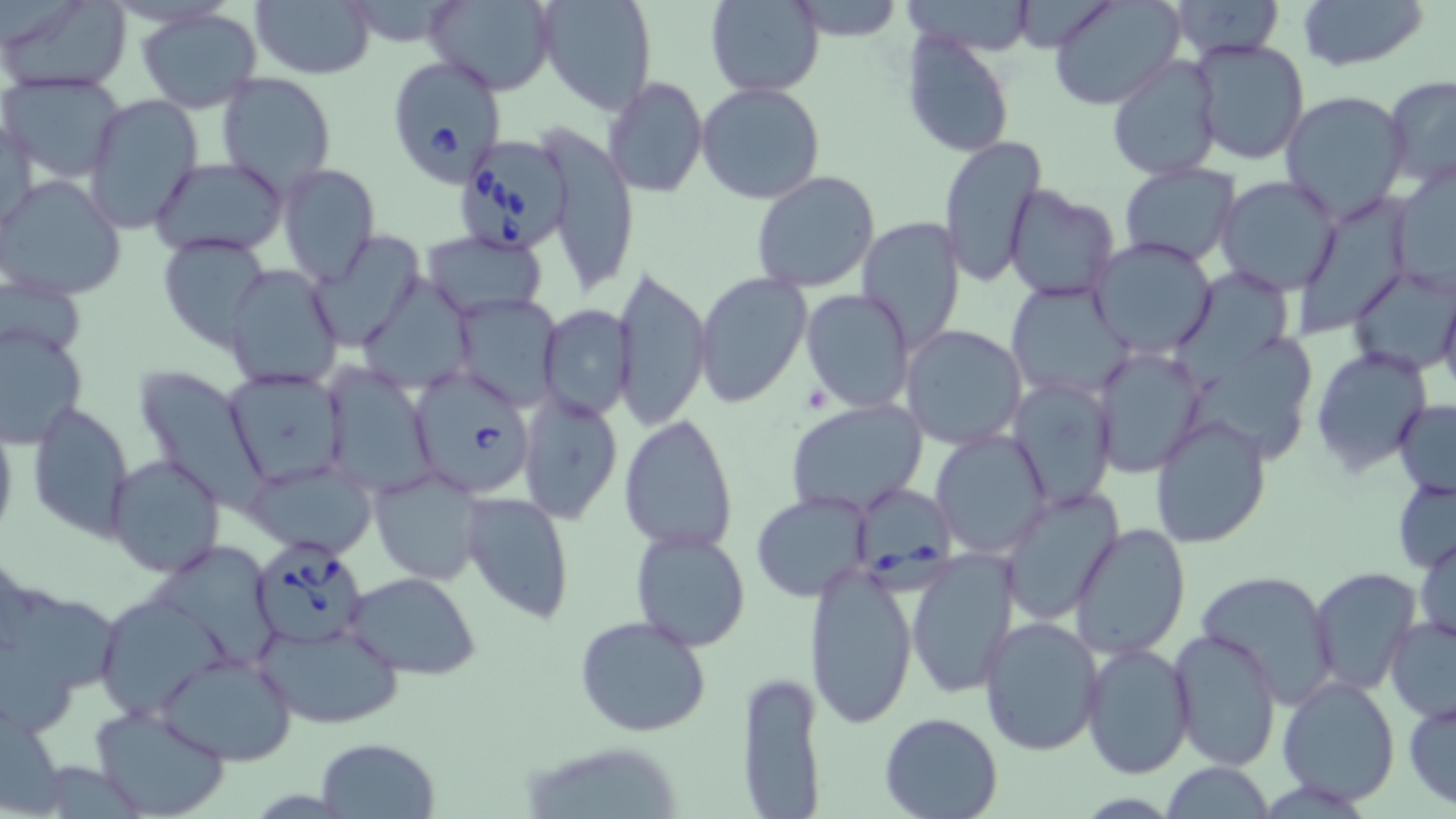

Approximate bounding boxes as named x1/y1/x2/y2 corners in pixels. Babesia divergens-infected red blood cell locations: (x1=384, y1=51, x2=506, y2=189), (x1=452, y1=130, x2=575, y2=257), (x1=405, y1=366, x2=535, y2=497), (x1=852, y1=480, x2=959, y2=596), (x1=249, y1=538, x2=368, y2=651). Platelet locations: (x1=802, y1=383, x2=829, y2=411). Uninfected red blood cell locations: (x1=1, y1=0, x2=130, y2=94), (x1=425, y1=0, x2=556, y2=94), (x1=537, y1=0, x2=657, y2=115), (x1=705, y1=0, x2=824, y2=97), (x1=1048, y1=0, x2=1182, y2=110), (x1=1298, y1=0, x2=1428, y2=70), (x1=1168, y1=1, x2=1285, y2=61), (x1=251, y1=2, x2=376, y2=79), (x1=787, y1=2, x2=909, y2=43), (x1=137, y1=8, x2=262, y2=114), (x1=900, y1=29, x2=1015, y2=160), (x1=1187, y1=38, x2=1311, y2=168), (x1=1105, y1=56, x2=1222, y2=183), (x1=215, y1=71, x2=337, y2=194), (x1=2, y1=74, x2=128, y2=182), (x1=1383, y1=74, x2=1456, y2=189), (x1=603, y1=76, x2=708, y2=199), (x1=696, y1=82, x2=826, y2=205), (x1=1282, y1=90, x2=1412, y2=224), (x1=81, y1=94, x2=202, y2=234), (x1=2, y1=113, x2=39, y2=234), (x1=543, y1=130, x2=641, y2=292), (x1=938, y1=136, x2=1047, y2=286), (x1=150, y1=157, x2=289, y2=257), (x1=277, y1=163, x2=380, y2=287), (x1=1118, y1=163, x2=1239, y2=269), (x1=1388, y1=163, x2=1456, y2=297), (x1=750, y1=171, x2=881, y2=294), (x1=0, y1=174, x2=127, y2=300), (x1=1214, y1=177, x2=1345, y2=296), (x1=1004, y1=184, x2=1121, y2=300), (x1=1302, y1=186, x2=1416, y2=334), (x1=856, y1=218, x2=969, y2=352), (x1=422, y1=231, x2=549, y2=319), (x1=308, y1=232, x2=426, y2=350), (x1=156, y1=233, x2=272, y2=350), (x1=1088, y1=237, x2=1218, y2=359), (x1=613, y1=263, x2=713, y2=431), (x1=1348, y1=264, x2=1455, y2=378), (x1=222, y1=265, x2=344, y2=390), (x1=693, y1=271, x2=813, y2=408), (x1=1, y1=275, x2=84, y2=356), (x1=1171, y1=275, x2=1296, y2=387), (x1=360, y1=280, x2=477, y2=394), (x1=1005, y1=280, x2=1133, y2=405), (x1=1439, y1=282, x2=1456, y2=403), (x1=800, y1=288, x2=915, y2=413), (x1=449, y1=294, x2=562, y2=411), (x1=539, y1=305, x2=635, y2=419), (x1=1, y1=323, x2=87, y2=446), (x1=899, y1=324, x2=1030, y2=450), (x1=1182, y1=343, x2=1312, y2=454), (x1=1311, y1=346, x2=1433, y2=474), (x1=1092, y1=347, x2=1206, y2=477), (x1=322, y1=366, x2=439, y2=497), (x1=132, y1=367, x2=269, y2=510), (x1=222, y1=368, x2=348, y2=487), (x1=1007, y1=379, x2=1117, y2=510), (x1=516, y1=391, x2=622, y2=524), (x1=786, y1=398, x2=926, y2=517), (x1=28, y1=401, x2=133, y2=538), (x1=1393, y1=401, x2=1456, y2=497), (x1=619, y1=413, x2=738, y2=552), (x1=1149, y1=413, x2=1273, y2=548), (x1=0, y1=420, x2=18, y2=543), (x1=931, y1=429, x2=1051, y2=560), (x1=105, y1=454, x2=225, y2=577), (x1=244, y1=457, x2=378, y2=558), (x1=368, y1=467, x2=485, y2=585), (x1=1392, y1=476, x2=1456, y2=573), (x1=998, y1=488, x2=1123, y2=621), (x1=751, y1=490, x2=873, y2=603), (x1=461, y1=491, x2=574, y2=625), (x1=1068, y1=524, x2=1190, y2=660), (x1=629, y1=527, x2=751, y2=653), (x1=1413, y1=534, x2=1455, y2=645), (x1=150, y1=543, x2=282, y2=665), (x1=907, y1=551, x2=1020, y2=699), (x1=803, y1=564, x2=919, y2=729), (x1=1310, y1=566, x2=1422, y2=694), (x1=1194, y1=568, x2=1339, y2=705), (x1=345, y1=572, x2=482, y2=677), (x1=20, y1=599, x2=125, y2=696), (x1=96, y1=604, x2=233, y2=717), (x1=575, y1=614, x2=712, y2=738), (x1=1385, y1=615, x2=1456, y2=723), (x1=978, y1=616, x2=1107, y2=757), (x1=255, y1=618, x2=406, y2=731), (x1=1169, y1=628, x2=1281, y2=770), (x1=1081, y1=642, x2=1195, y2=777), (x1=156, y1=651, x2=299, y2=766), (x1=734, y1=673, x2=827, y2=816), (x1=1276, y1=676, x2=1401, y2=806), (x1=1404, y1=695, x2=1456, y2=810), (x1=90, y1=705, x2=231, y2=818), (x1=878, y1=712, x2=1003, y2=819), (x1=315, y1=737, x2=439, y2=817), (x1=34, y1=760, x2=142, y2=816), (x1=1161, y1=760, x2=1274, y2=818). Slide-level diagnosis: Babesia divergens. Single field of view. Thin blood smear. Image is 1456×819 pixels. Light microscopy. Captured at 1000x magnification. May-Grünwald-Giemsa-stained preparation.